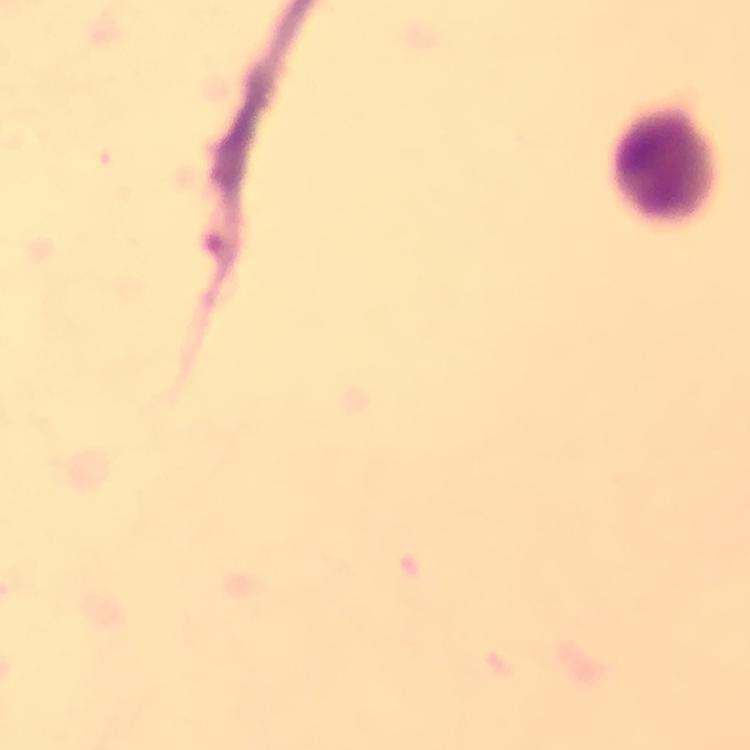

capture = smartphone camera through the microscope
stain = Giemsa
image size = 750×750 pixels
magnification = 100x
leukocyte locations = approximate object centers, in pixels from the top-left corner: (x=666, y=163)
cropped from = one field of view
immersion oil = applied
preparation = thick smear
malaria parasites = none seen
context = from a diagnostic examination for malaria